Find the red blood cells and label each as Plasmodium falciparum-infected, uninfected, or of indeterminate infection status.
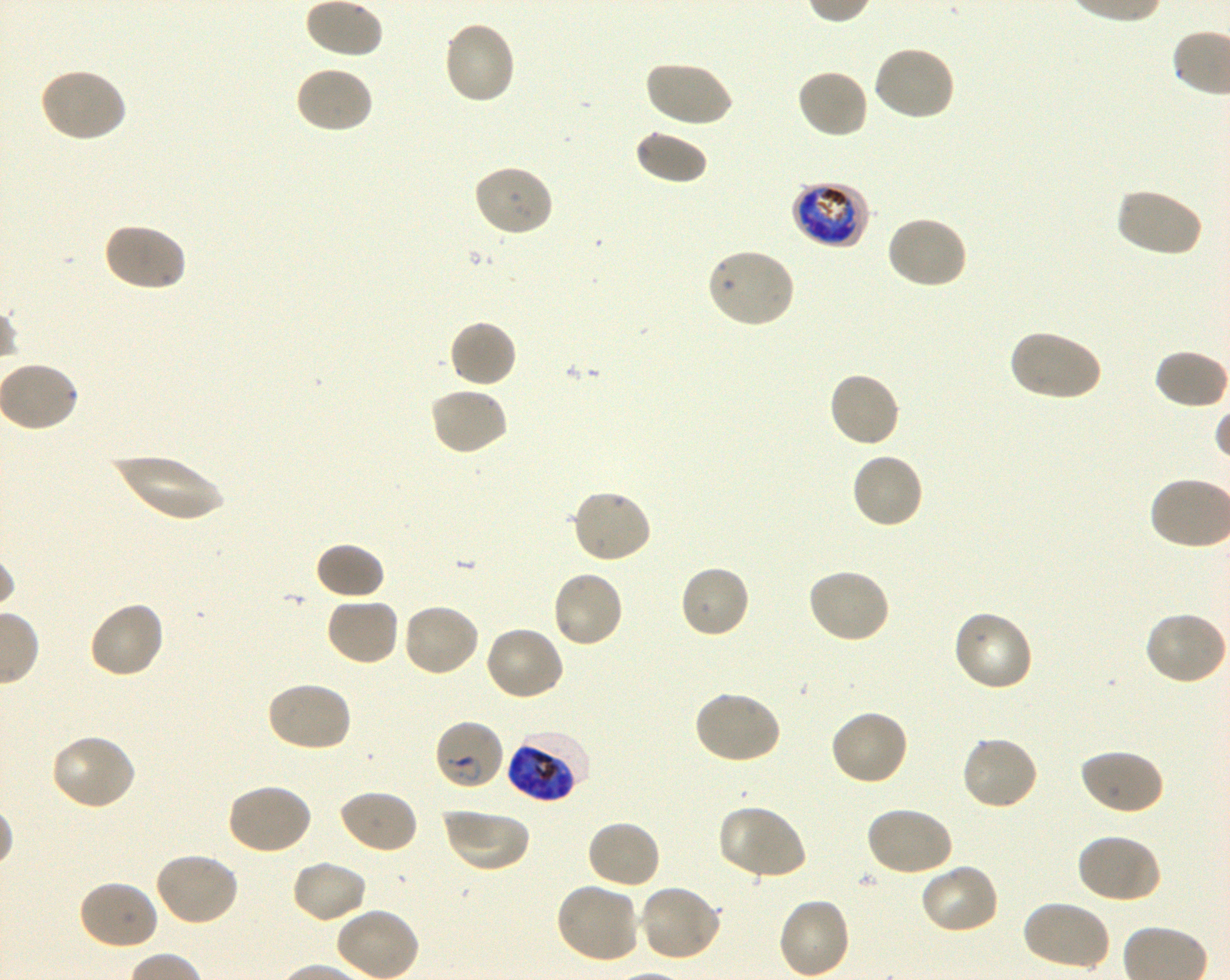

Approximate bounding rectangles given as corner coordinates in pixels from the top-left. Not every red blood cell is marked. A life-cycle stage — or a range of stages, where the recorded stages span more than one — follows each staged infected red blood cell.
Infected red blood cells: (x1=790, y1=180, x2=869, y2=249) late trophozoite to late schizont; (x1=433, y1=718, x2=505, y2=792) ring; (x1=508, y1=730, x2=589, y2=803) late trophozoite to late schizont.
Uninfected red blood cells: (x1=302, y1=0, x2=388, y2=59), (x1=442, y1=21, x2=517, y2=106), (x1=872, y1=43, x2=957, y2=121), (x1=644, y1=59, x2=733, y2=129), (x1=293, y1=65, x2=375, y2=135), (x1=37, y1=67, x2=127, y2=143), (x1=796, y1=67, x2=870, y2=139), (x1=633, y1=128, x2=709, y2=186), (x1=472, y1=164, x2=555, y2=237), (x1=1114, y1=186, x2=1204, y2=258), (x1=885, y1=214, x2=968, y2=290), (x1=102, y1=221, x2=187, y2=293), (x1=705, y1=247, x2=796, y2=329), (x1=448, y1=319, x2=518, y2=389), (x1=1007, y1=328, x2=1103, y2=403), (x1=1153, y1=349, x2=1229, y2=410), (x1=827, y1=370, x2=902, y2=448), (x1=429, y1=386, x2=510, y2=456), (x1=850, y1=452, x2=924, y2=530), (x1=110, y1=454, x2=228, y2=520), (x1=570, y1=488, x2=653, y2=565), (x1=313, y1=541, x2=386, y2=601), (x1=678, y1=564, x2=751, y2=639), (x1=806, y1=567, x2=890, y2=645), (x1=550, y1=570, x2=624, y2=650), (x1=324, y1=597, x2=401, y2=667), (x1=87, y1=600, x2=166, y2=680), (x1=401, y1=603, x2=481, y2=678), (x1=952, y1=610, x2=1034, y2=693), (x1=1144, y1=611, x2=1229, y2=687), (x1=484, y1=625, x2=567, y2=702), (x1=264, y1=680, x2=353, y2=754), (x1=693, y1=689, x2=783, y2=766), (x1=829, y1=709, x2=909, y2=787), (x1=50, y1=733, x2=138, y2=811), (x1=960, y1=735, x2=1040, y2=811), (x1=1078, y1=748, x2=1164, y2=816), (x1=225, y1=782, x2=313, y2=857), (x1=336, y1=788, x2=418, y2=854), (x1=864, y1=804, x2=954, y2=877), (x1=717, y1=805, x2=809, y2=883), (x1=441, y1=807, x2=530, y2=874), (x1=585, y1=819, x2=662, y2=891), (x1=1075, y1=832, x2=1162, y2=904), (x1=153, y1=850, x2=240, y2=926), (x1=289, y1=860, x2=368, y2=925), (x1=918, y1=862, x2=1001, y2=936), (x1=77, y1=879, x2=160, y2=951), (x1=555, y1=882, x2=640, y2=965), (x1=639, y1=884, x2=724, y2=964), (x1=777, y1=896, x2=852, y2=979), (x1=1020, y1=899, x2=1111, y2=972).
No red blood cells of indeterminate infection status observed.

donor blood group = O+
stain = Giemsa
image size = 1230×980 pixels
culture = shaking in-vitro Plasmodium falciparum strain 3D7
preparation = thin blood smear
field of view = one from this slide
objective = 100x, oil immersion, numerical aperture 1.30